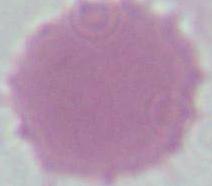

magnification: 1000x
modality: photomicrograph
identification: red blood cell